State which parasite is depicted.
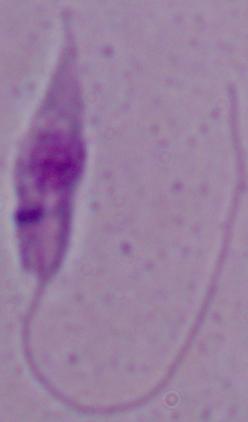

This is Leishmania.

{
  "magnification": "1000x",
  "modality": "photomicrograph"
}